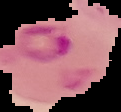 The area outside the segmented cell region is set to black. Image is 121×112 pixels. Malaria status: parasitized. From a thin blood film.